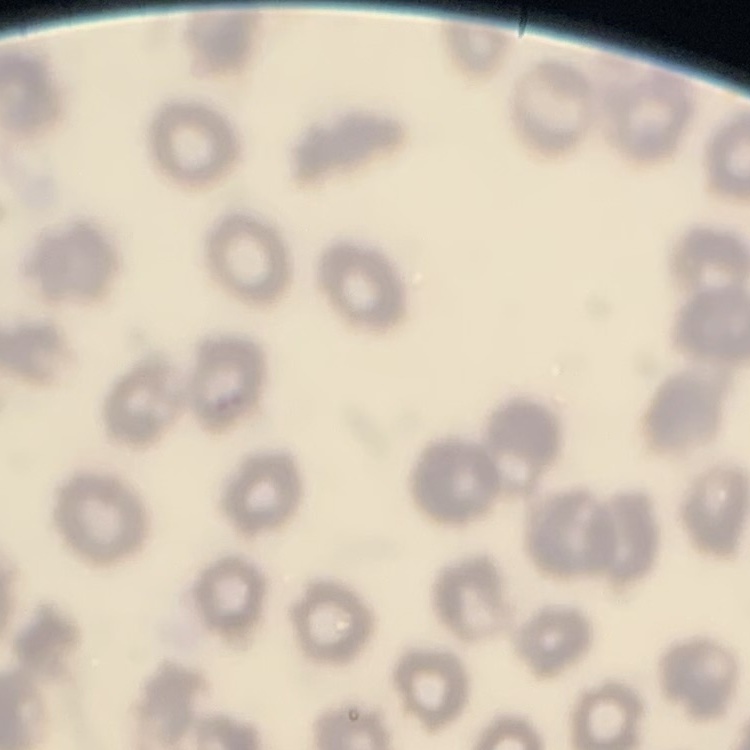
Summary:
  - Red blood cell morphology: no rouleaux formation
  - Image type: one tile cut from a larger photomicrograph
  - Preparation: thin blood film
  - Stain: Field's or Giemsa